Report the malaria status of this cell.
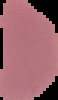

Uninfected.

From a thin blood smear. Image is 58×100 pixels. Segmented cell region on a black background.